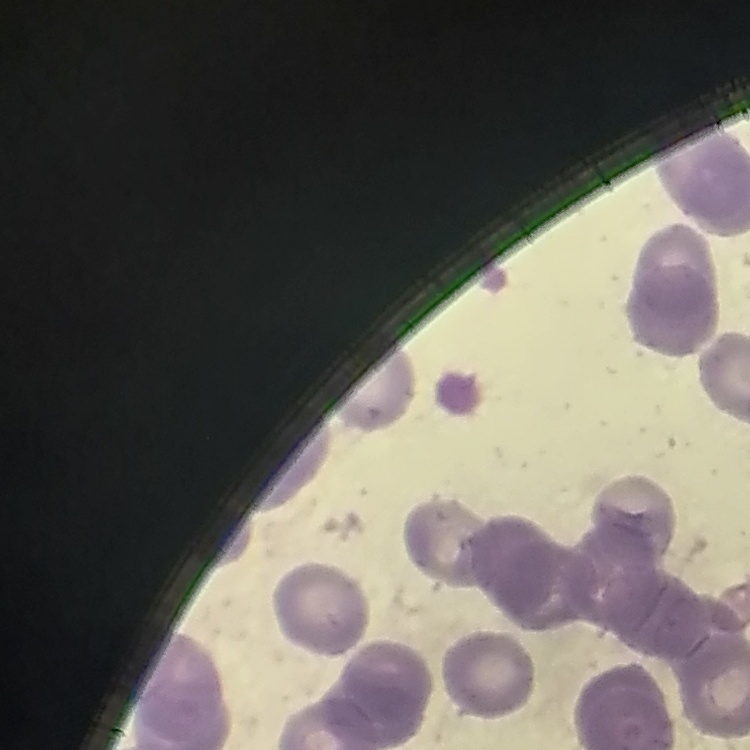

The red blood cells show rouleaux formation. Stained with either Field's or Giemsa. Thin peripheral smear. Square crop of a larger photomicrograph.